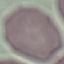
Malaria status: uninfected. Thin blood film. Acquired by smartphone through the microscope eyepiece. Giemsa stain. Automatically extracted cell patch, resized to 64 × 64 pixels.